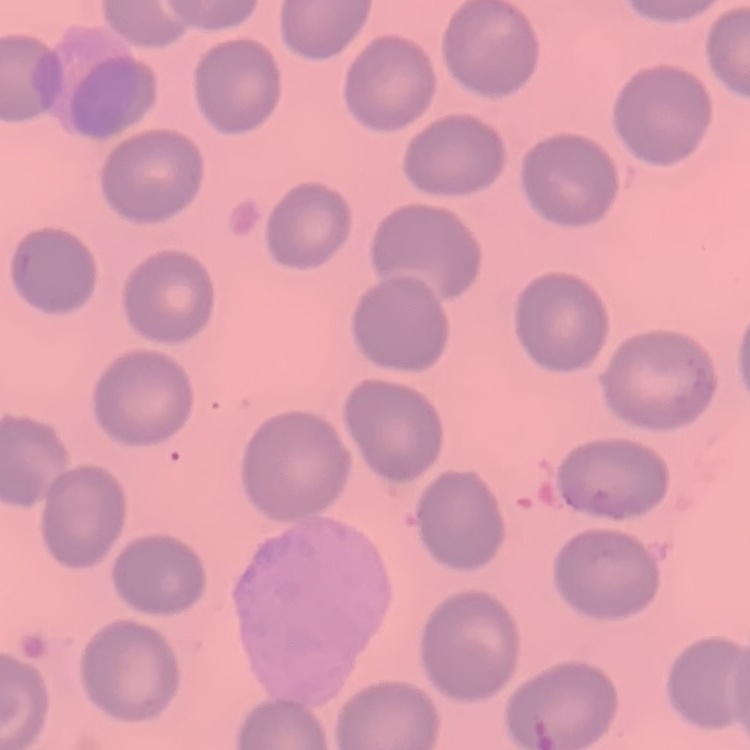

The red blood cells exhibit no rouleaux formation. One tile cut from a larger photomicrograph. Field's or Giemsa stain. Thin blood smear.